State which parasite is depicted.
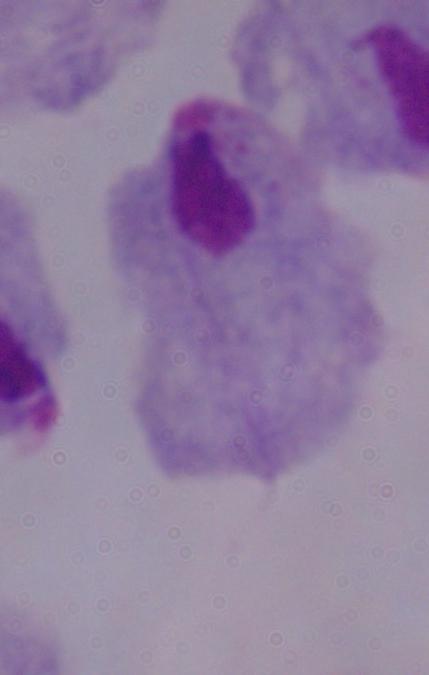
This is a trichomonad.

Summary:
  - Magnification: 1000x
  - Modality: micrograph